Report the malaria status of this cell.
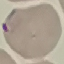
Parasitized.

Thin blood smear. Giemsa stain. Cell patch, automatically extracted from a larger field of view and resized to 64 × 64 pixels. Photographed with a smartphone camera at the microscope eyepiece.